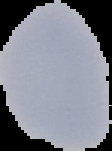
Segmented cell region on a black background. Image is 112×151 pixels. Result: no malaria parasites seen. From a thin blood film.